Assess this cell for malaria.
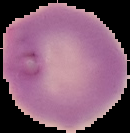
It is parasitized.

Summary:
  - Preparation: thin blood film
  - Image size: 130×133 pixels
  - Image type: segmented cell region on a black background